Classify this cell by malaria status.
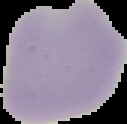
It is uninfected.

Summary:
  - Image type: cell region segmented out of the field of view; surrounding area masked to black
  - Image size: 127×124 pixels
  - Preparation: thin blood smear